Assess this cell for malaria.
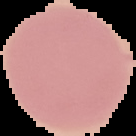
It is uninfected.

From a thin blood smear. Image is 136×136 pixels. Segmented cell region on a black background.